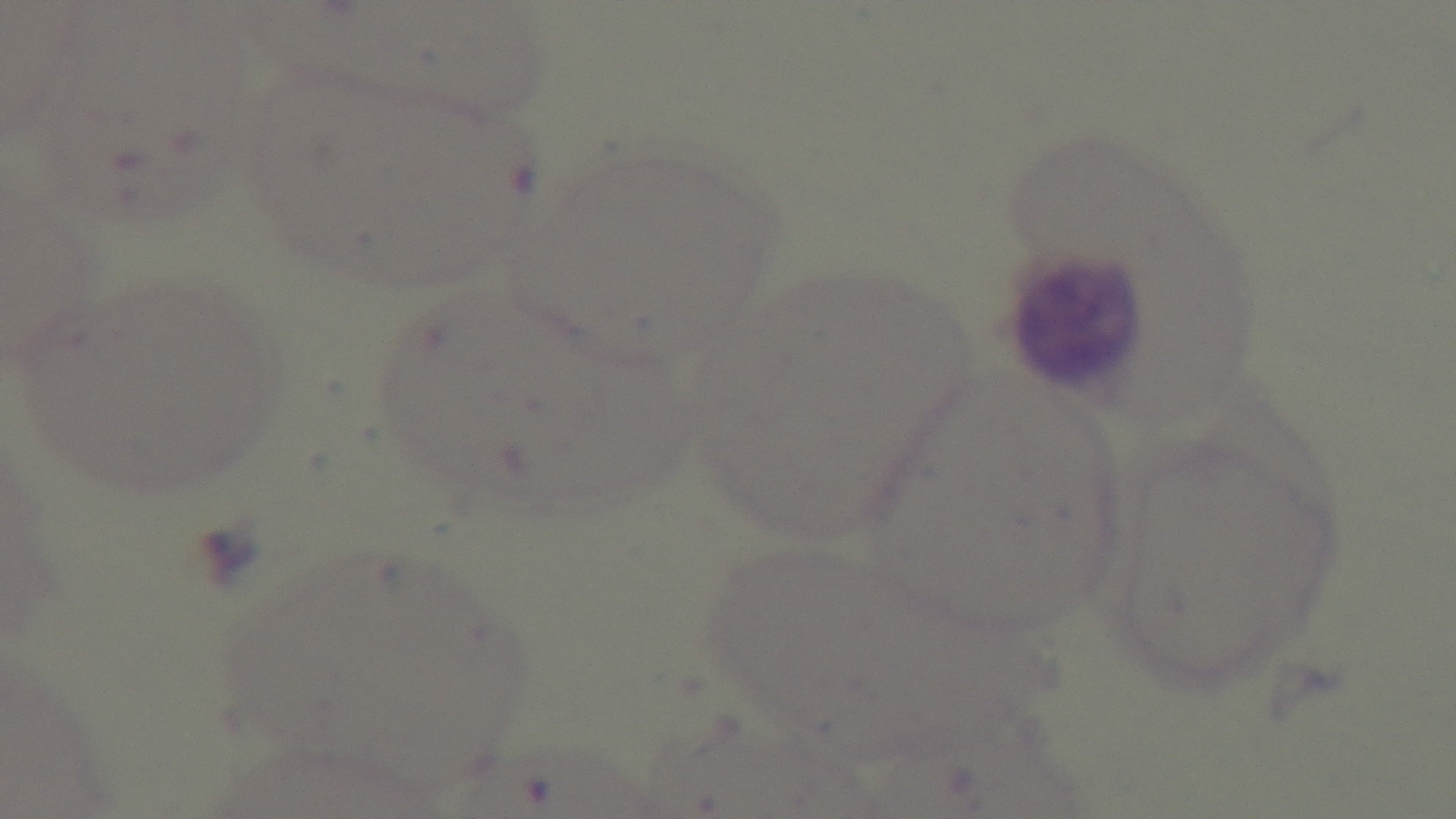

capture = mounted 4K digital camera
modality = light microscopy
preparation = thin blood film
stain = Giemsa
field of view = one from the slide
malaria status = negative
objective = 100x oil immersion